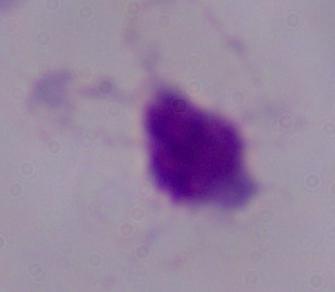

Summary:
  - Identification: trichomonad
  - Magnification: 1000x
  - Modality: photomicrograph